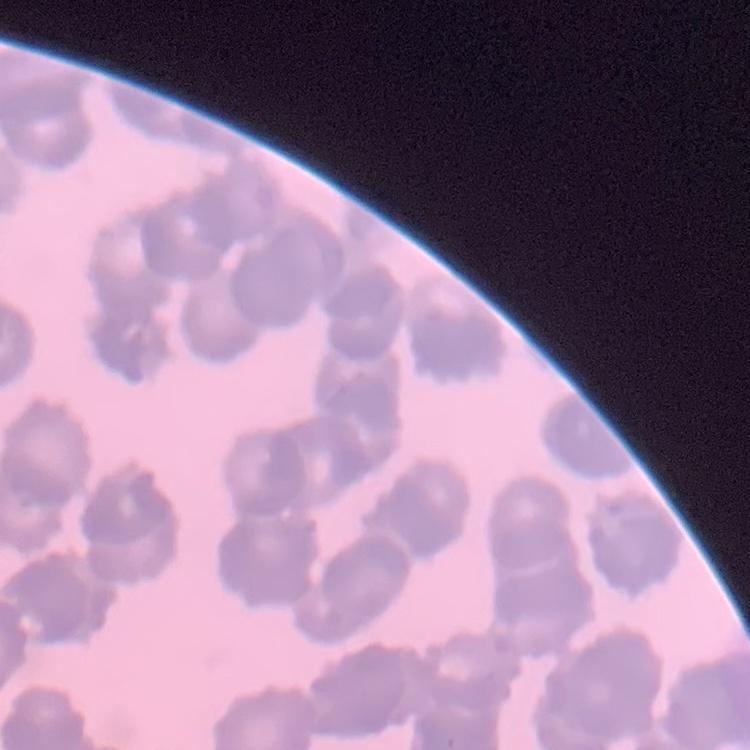

The red blood cells exhibit rouleaux formation. Square crop of a larger photomicrograph. Stained with either Field's or Giemsa. Thin blood film.